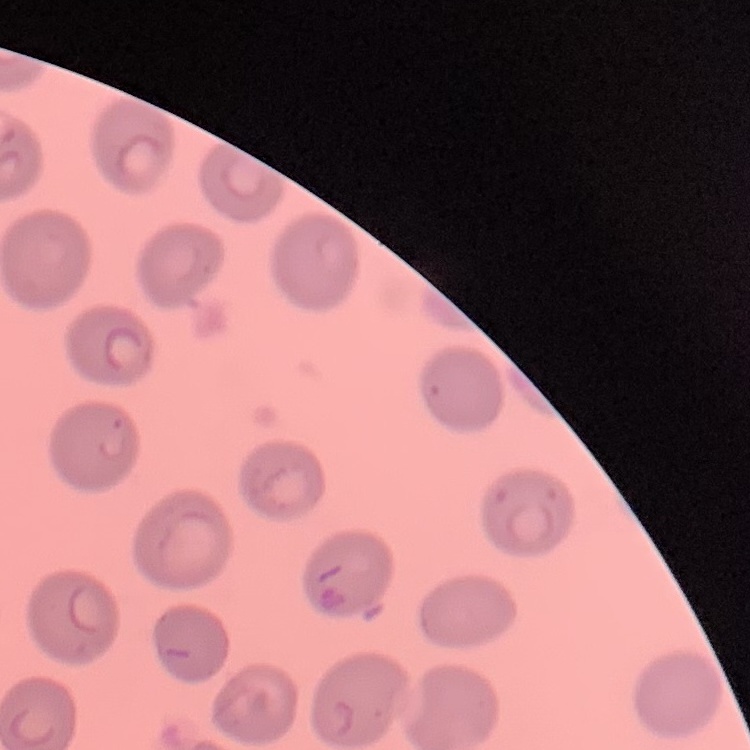
Summary:
  - Red blood cell morphology: no rouleaux formation
  - Image type: one tile cut from a larger photomicrograph
  - Stain: Field's or Giemsa
  - Preparation: thin peripheral smear